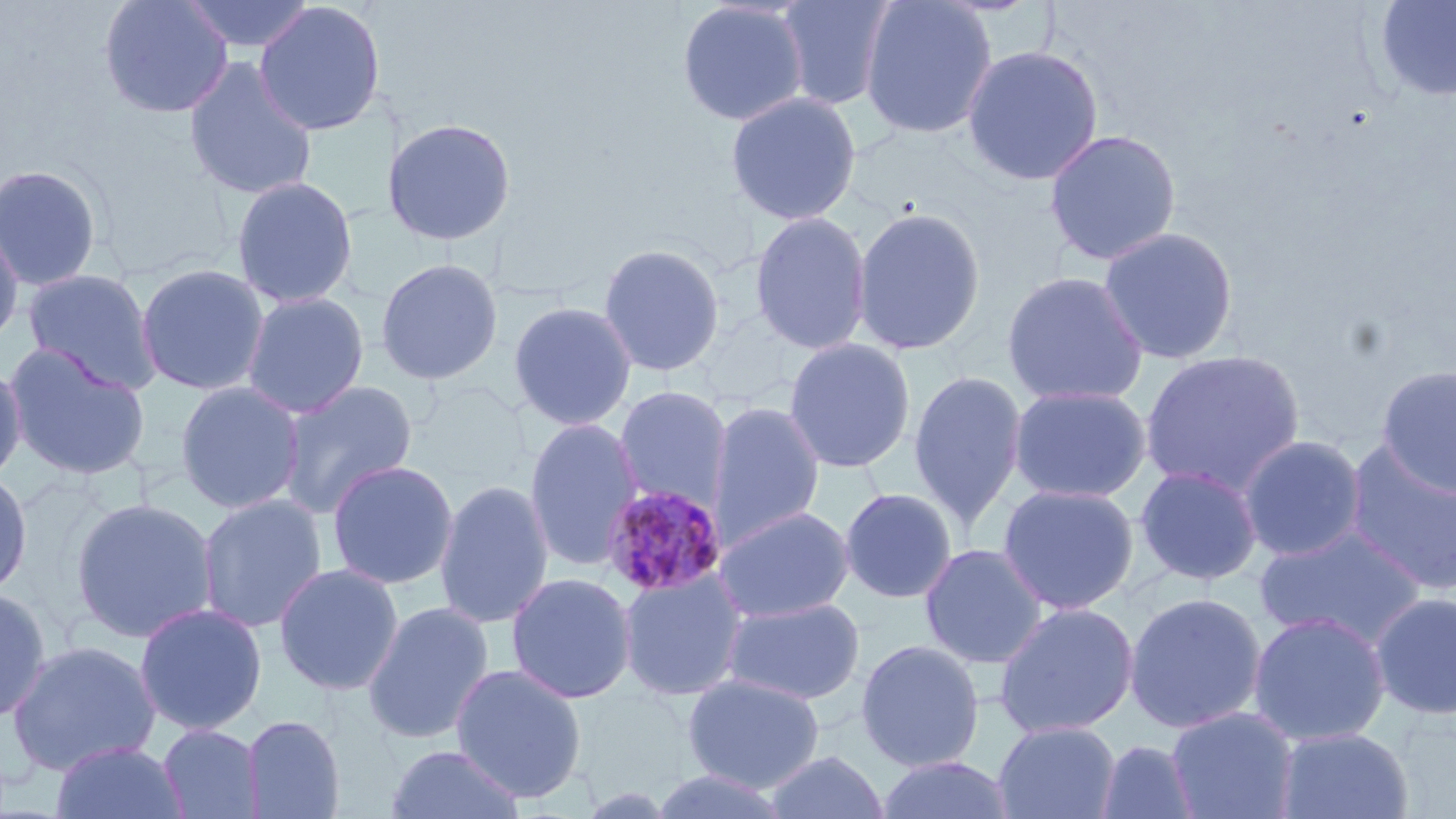

slide-level diagnosis = Plasmodium malariae
preparation = thin blood smear
uninfected red blood cell locations = approximate bounding boxes as (x1, y1, x2, y2) in pixels: (98, 0, 234, 118), (180, 0, 316, 55), (676, 0, 809, 127), (775, 0, 898, 110), (860, 0, 998, 139), (253, 1, 387, 136), (1374, 1, 1456, 102), (962, 44, 1104, 186), (182, 57, 319, 201), (725, 91, 862, 226), (381, 116, 517, 247), (1043, 128, 1183, 266), (0, 163, 104, 292), (230, 175, 358, 309), (852, 206, 986, 356), (749, 210, 872, 355), (0, 219, 25, 351), (1097, 225, 1239, 365), (597, 242, 725, 378), (375, 257, 504, 385), (134, 262, 271, 396), (21, 267, 162, 394), (1001, 270, 1149, 407), (241, 292, 369, 419), (508, 301, 637, 431), (782, 338, 917, 473), (3, 342, 152, 481), (1139, 349, 1305, 497), (0, 361, 27, 487), (1376, 365, 1456, 496), (908, 368, 1028, 529), (276, 379, 419, 520), (174, 380, 305, 514), (614, 384, 732, 513), (1008, 384, 1152, 503), (708, 401, 825, 547), (524, 417, 645, 571), (1238, 434, 1368, 562), (1342, 439, 1456, 597), (325, 459, 460, 590), (1134, 464, 1264, 587), (0, 468, 33, 600), (434, 478, 554, 630), (997, 482, 1140, 616), (838, 487, 958, 603), (196, 494, 328, 633), (69, 497, 219, 644), (713, 505, 856, 624), (1254, 526, 1427, 651), (919, 543, 1049, 669), (273, 562, 405, 696), (617, 568, 749, 702), (505, 572, 637, 705), (0, 587, 51, 725), (1369, 591, 1456, 721), (1124, 592, 1267, 734), (721, 596, 866, 704), (361, 601, 495, 745), (992, 601, 1140, 739), (133, 602, 268, 736), (1247, 611, 1391, 746), (855, 639, 985, 772), (5, 640, 162, 775), (450, 664, 587, 802), (681, 673, 826, 792), (1165, 707, 1301, 819), (242, 714, 346, 818), (993, 721, 1121, 819), (158, 723, 264, 818), (1274, 727, 1414, 818), (1095, 739, 1199, 819), (50, 740, 189, 819), (383, 743, 526, 819), (762, 749, 890, 819), (874, 755, 1018, 818), (648, 769, 793, 818)
image size = 1456×819 pixels
magnification = 1000x
modality = optical microscopy
stain = May-Grünwald-Giemsa
Plasmodium malariae-infected red blood cell locations = approximate bounding boxes as (x1, y1, x2, y2) in pixels: (600, 483, 728, 598)
field of view = one of a larger specimen